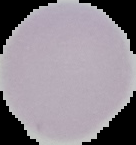

image size = 136×145 pixels
preparation = thin blood film
malaria status = uninfected
image type = cell region segmented out of the field of view; surrounding area masked to black